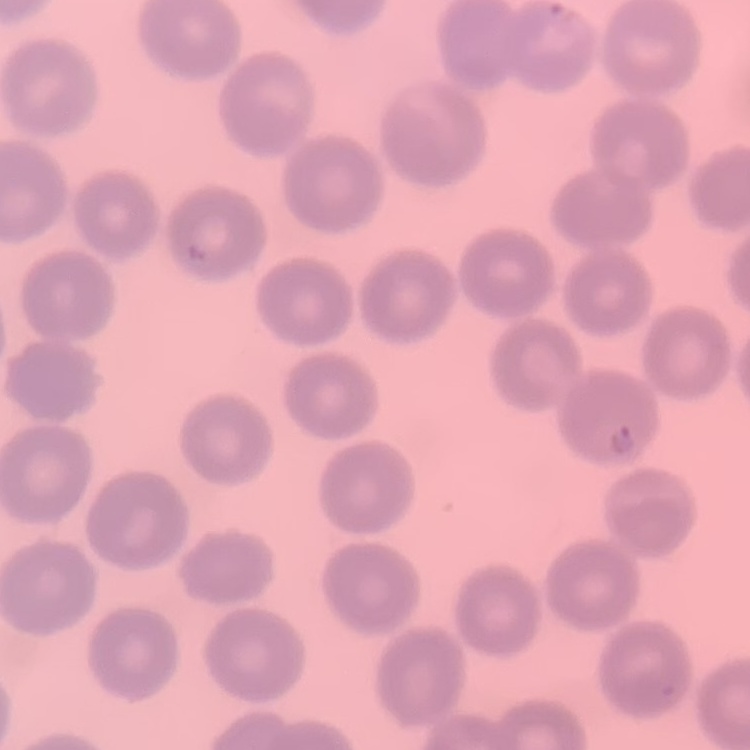

erythrocyte morphology = no rouleaux formation
image type = square crop of a larger photomicrograph
stain = Field's or Giemsa
preparation = thin blood smear